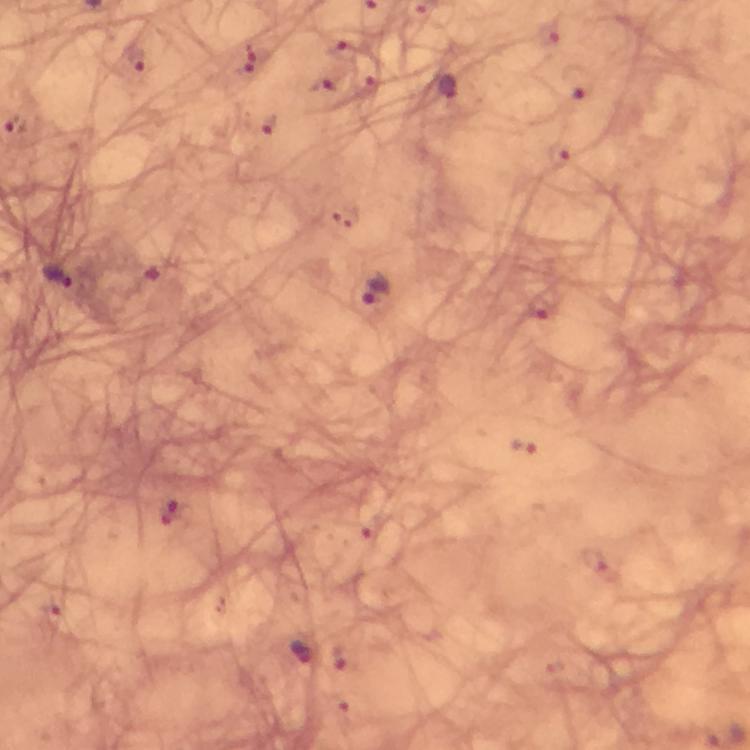
image size = 750×750 pixels
cropped from = a single field of view
context = from a diagnostic examination for malaria
stain = Giemsa
preparation = thick blood film
capture = smartphone mounted on the microscope
magnification = 100x
Plasmodium parasite locations = approximate object centers, in pixels from the top-left corner: (x=136, y=58), (x=252, y=60), (x=449, y=88), (x=266, y=125), (x=558, y=154), (x=60, y=275), (x=375, y=290), (x=543, y=308), (x=523, y=446), (x=171, y=512), (x=51, y=613), (x=301, y=654)
immersion oil = applied